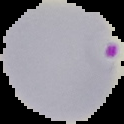 Segmented cell region on a black background. Result: malaria parasites identified. Image is 124×124 pixels. From a thin blood film.